Identify the parasite.
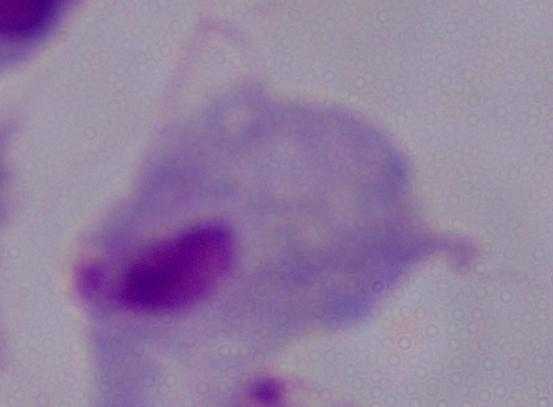
This is a trichomonad.

Summary:
  - Modality: micrograph
  - Magnification: 1000x